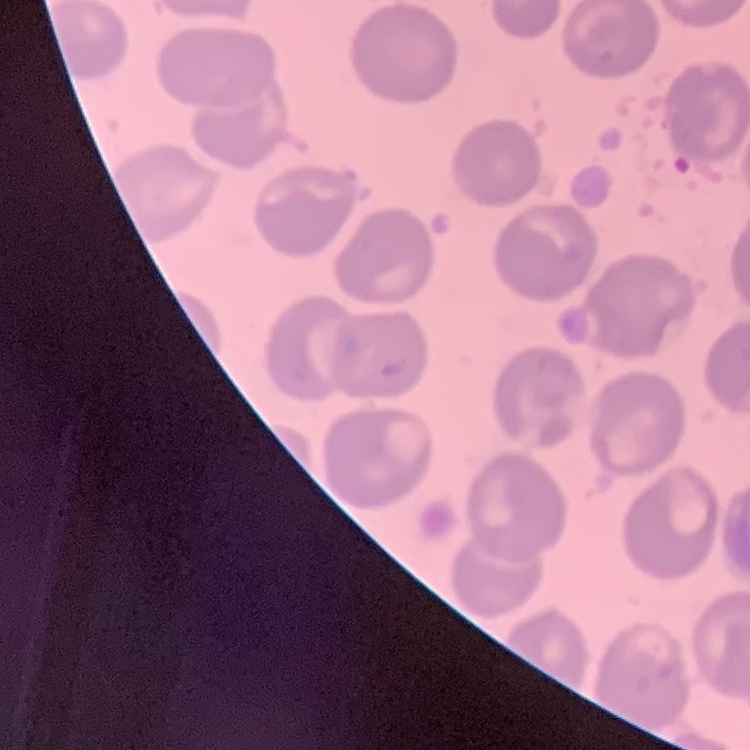

The red blood cells exhibit no rouleaux formation. Thin blood smear. One tile cut from a larger photomicrograph. Field's or Giemsa stain.